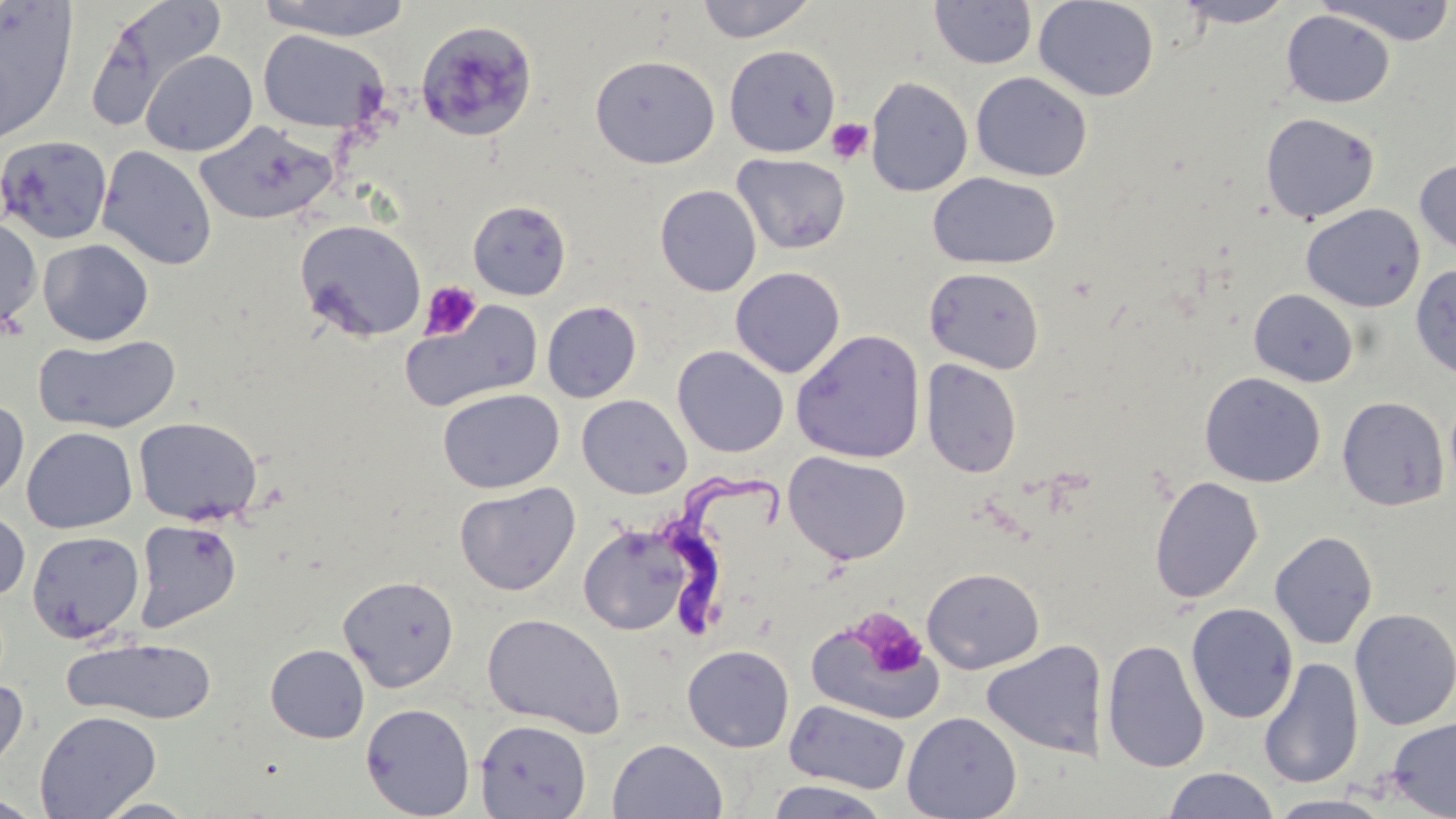 Approximate bounding boxes as (x1,y1)-(x2,y2) corner pairs in pixels. Platelet locations: (826,118)-(873,165), (420,280)-(482,341), (860,614)-(927,678). Trypanosoma brucei locations: (658,460)-(794,636). Uninfected red blood cell locations: (254,0)-(416,41), (695,0)-(819,43), (1033,0)-(1159,102), (1173,0)-(1297,28), (1318,0)-(1456,47), (1,1)-(78,144), (82,1)-(225,131), (929,1)-(1037,70), (1281,9)-(1395,108), (417,24)-(547,141), (257,30)-(389,133), (723,44)-(841,158), (140,50)-(258,156), (589,54)-(721,169), (971,72)-(1092,182), (865,76)-(973,197), (1260,112)-(1380,223), (195,120)-(337,225), (1,134)-(113,245), (97,146)-(217,270), (732,153)-(851,255), (1414,159)-(1456,256), (927,172)-(1061,269), (654,184)-(761,296), (467,200)-(572,301), (1301,203)-(1425,312), (0,215)-(43,334), (295,218)-(427,342), (38,239)-(154,346), (1410,263)-(1456,378), (729,267)-(845,379), (924,267)-(1044,374), (1248,289)-(1359,387), (542,300)-(642,402), (400,301)-(544,414), (790,329)-(926,463), (32,335)-(182,434), (672,345)-(789,458), (921,358)-(1022,478), (1199,372)-(1326,487), (438,388)-(564,494), (577,394)-(692,499), (1337,395)-(1449,511), (0,398)-(29,503), (133,416)-(263,526), (22,427)-(138,533), (783,451)-(912,566), (1149,475)-(1264,604), (454,482)-(580,596), (0,507)-(30,603), (133,519)-(242,633), (578,521)-(697,636), (27,530)-(144,643), (1270,530)-(1378,649), (921,567)-(1044,674), (338,574)-(459,692), (1185,603)-(1299,724), (1350,607)-(1456,730), (805,610)-(944,727), (481,613)-(626,737), (62,636)-(218,725), (1102,639)-(1210,773), (982,640)-(1108,759), (265,644)-(369,743), (682,644)-(795,753), (1258,657)-(1363,789), (0,678)-(29,784), (784,698)-(911,794), (360,703)-(475,818), (34,710)-(162,818), (902,711)-(1022,819), (1385,717)-(1455,819), (475,719)-(591,818), (607,738)-(728,819), (1162,767)-(1280,818), (763,779)-(892,818), (0,793)-(46,817), (1269,794)-(1392,819), (91,797)-(203,819). Slide-level diagnosis: Trypanosoma brucei. May-Grünwald-Giemsa-stained preparation. Light microscopy. Captured at 1000x magnification. Thin blood film. Image is 1456×819 pixels. One field of a larger specimen.